Name the blood parasite species.
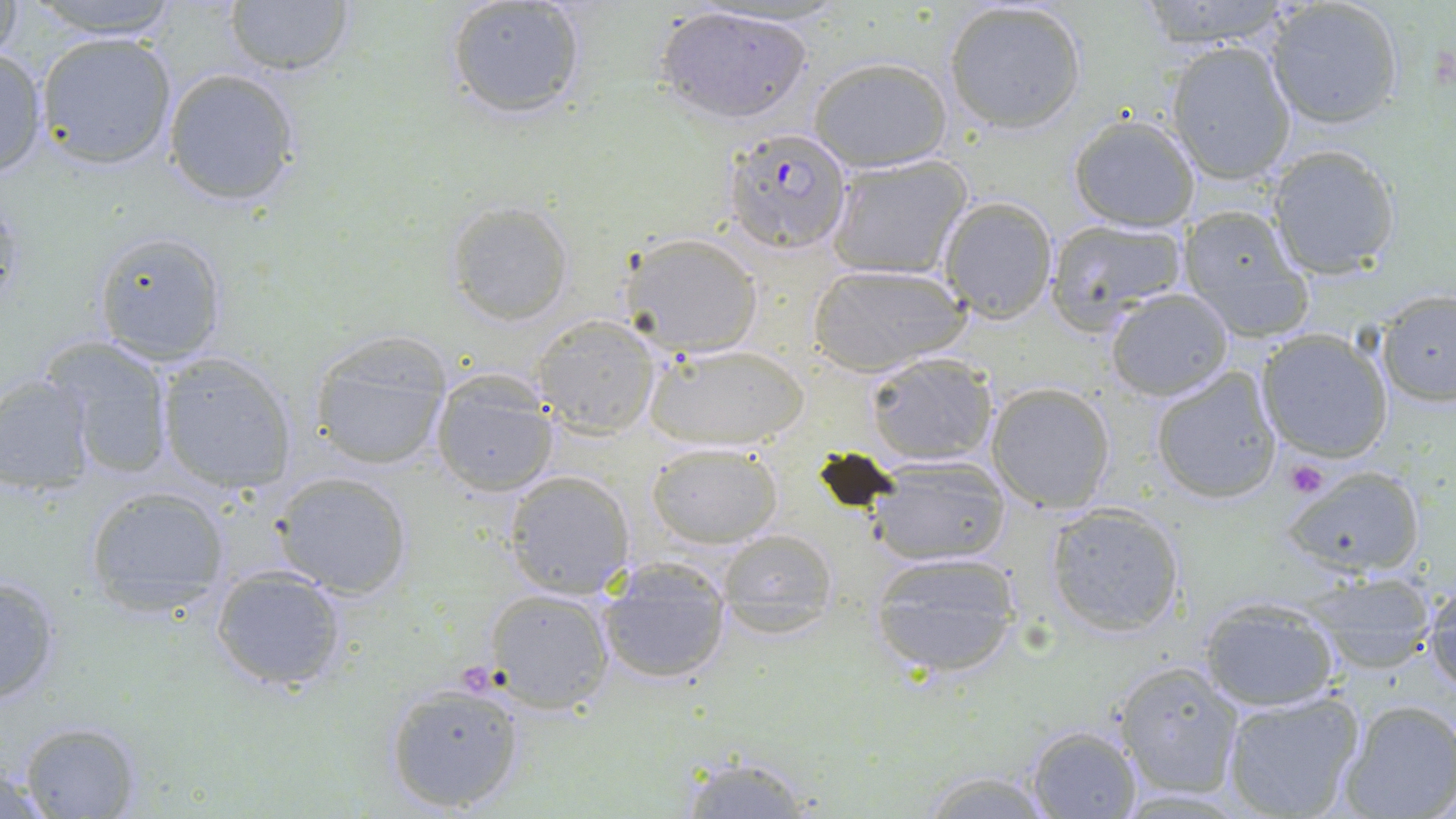
Plasmodium falciparum.

Summary:
  - Coordinate format: approximate bounding boxes as (x1, y1, x2, y2) in pixels
  - Plasmodium falciparum-infected red blood cell locations: (725, 128, 854, 254)
  - Platelet locations: (1284, 457, 1329, 498)
  - Uninfected red blood cell locations: (1, 0, 25, 69), (20, 0, 183, 39), (222, 0, 355, 76), (1136, 0, 1302, 48), (1263, 0, 1402, 130), (443, 1, 589, 123), (942, 1, 1089, 134), (653, 5, 817, 126), (35, 31, 179, 171), (1165, 41, 1297, 183), (0, 46, 48, 179), (809, 56, 953, 172), (162, 68, 302, 206), (1067, 114, 1201, 231), (1266, 144, 1402, 279), (824, 154, 974, 279), (937, 197, 1059, 321), (445, 201, 574, 324), (1176, 206, 1317, 344), (1044, 219, 1188, 329), (91, 231, 229, 364), (620, 233, 766, 355), (807, 263, 969, 373), (1105, 288, 1234, 402), (1376, 289, 1456, 407), (531, 313, 662, 437), (1257, 328, 1395, 463), (309, 333, 454, 472), (45, 336, 175, 477), (645, 341, 806, 451), (155, 351, 299, 493), (864, 354, 999, 466), (1149, 366, 1281, 504), (0, 373, 98, 491), (430, 373, 557, 496), (985, 380, 1116, 513), (647, 440, 782, 547), (865, 452, 1012, 566), (1283, 462, 1427, 578), (274, 471, 412, 597), (503, 471, 632, 598), (84, 487, 234, 614), (1045, 504, 1185, 637), (716, 530, 837, 613), (866, 551, 1024, 682), (209, 567, 348, 693), (0, 571, 66, 707), (1302, 572, 1441, 674), (1425, 581, 1456, 698), (597, 588, 730, 685), (484, 589, 614, 713), (1196, 596, 1343, 712), (714, 601, 840, 639), (1114, 661, 1247, 800), (383, 680, 528, 813), (1220, 692, 1364, 818), (1338, 699, 1456, 819), (14, 720, 144, 818), (1026, 725, 1142, 818), (670, 752, 824, 815), (912, 768, 1060, 819)
  - Field of view: one of a larger specimen
  - Magnification: 1000x
  - Preparation: thin blood smear
  - Stain: May-Grünwald-Giemsa
  - Modality: light microscopy
  - Image size: 1456×819 pixels